Assess this cell for malaria.
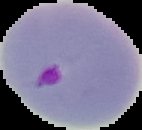

It is parasitized.

From a thin blood smear. The area outside the segmented cell region is set to black. Image is 142×130 pixels.